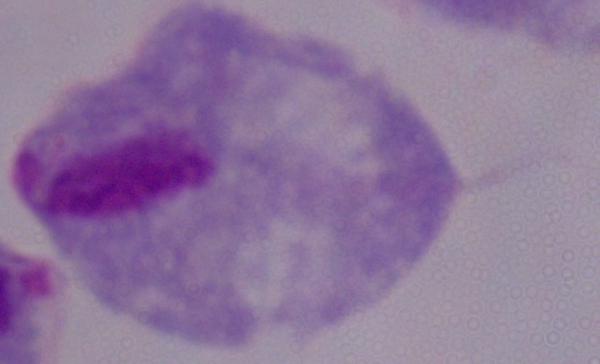 Photomicrograph. A trichomonad is seen. 1000x magnification.